Classify this cell by malaria status.
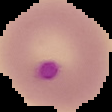
Parasitized.

From a thin blood smear. The area outside the segmented cell region is set to black. Image is 112×112 pixels.